Locate every Plasmodium parasite.
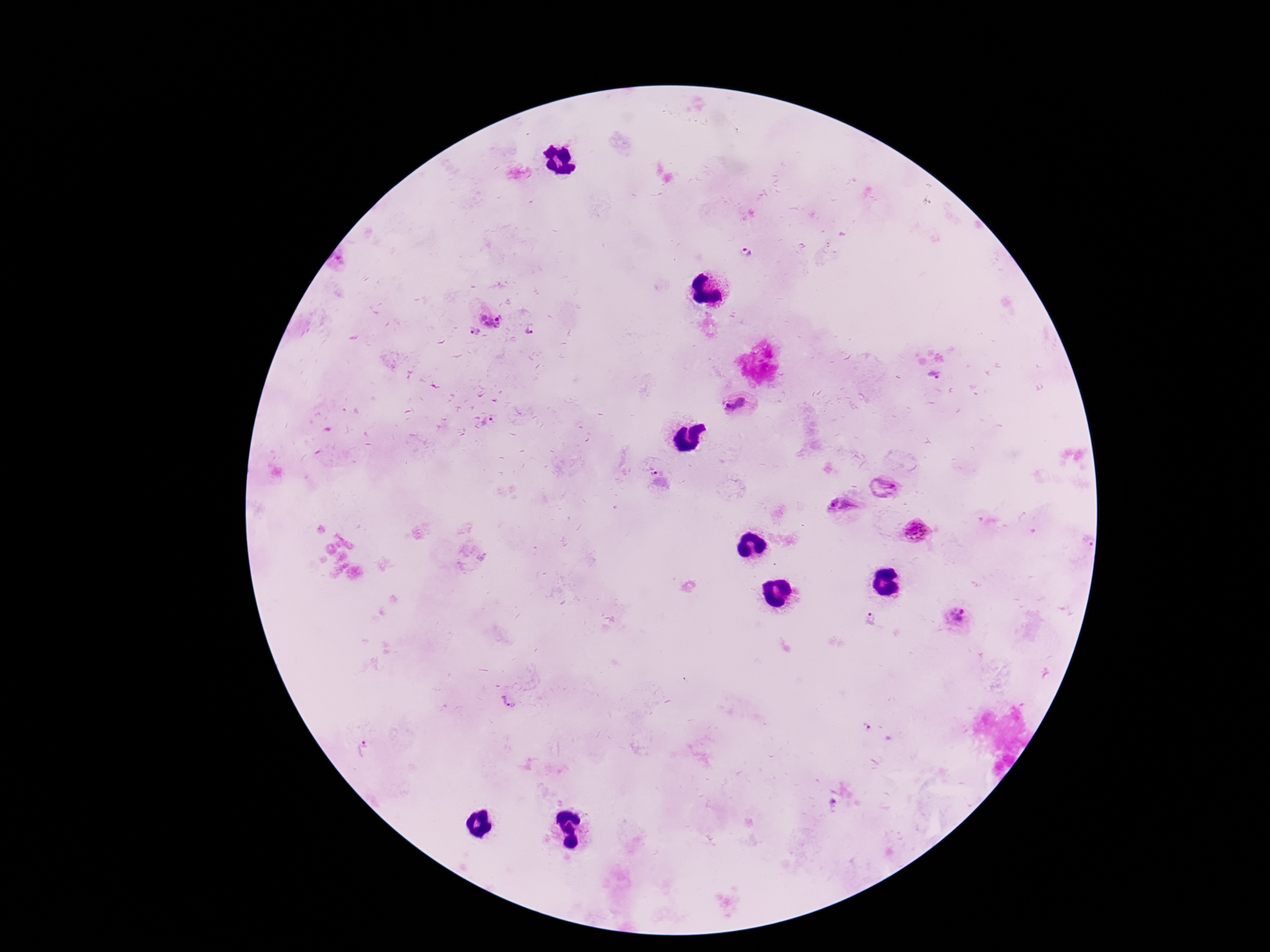

Approximate centers as (x, y) in pixels.
Plasmodium parasites: (747, 253), (490, 318), (475, 331), (531, 331), (934, 375), (736, 406), (489, 421), (651, 471), (882, 489), (833, 502), (847, 506), (915, 532), (1088, 542), (957, 618), (870, 619), (508, 702), (866, 727), (365, 750), (833, 802).

preparation: thick peripheral-blood smear
patient_malaria_status: infected
capture: smartphone camera through the microscope eyepiece
stain: Giemsa
magnification: 100x
image_size: 1270×952 pixels
field_of_view: single